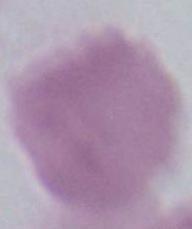

{
  "magnification": "1000x",
  "identification": "erythrocyte",
  "modality": "photomicrograph"
}